Identify the parasite.
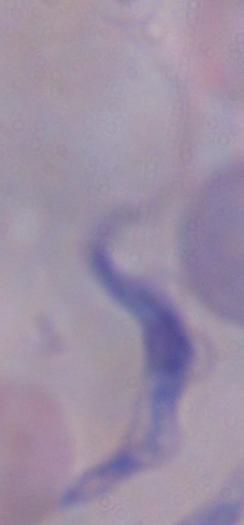
A trypanosome.

modality = micrograph
magnification = 1000x